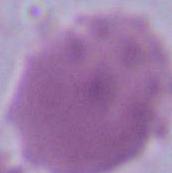
identification = red blood cell
modality = photomicrograph
magnification = 1000x